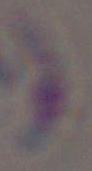
1000x magnification. Micrograph. Toxoplasma gondii is shown.